Give the position of every Plasmodium parasite visible.
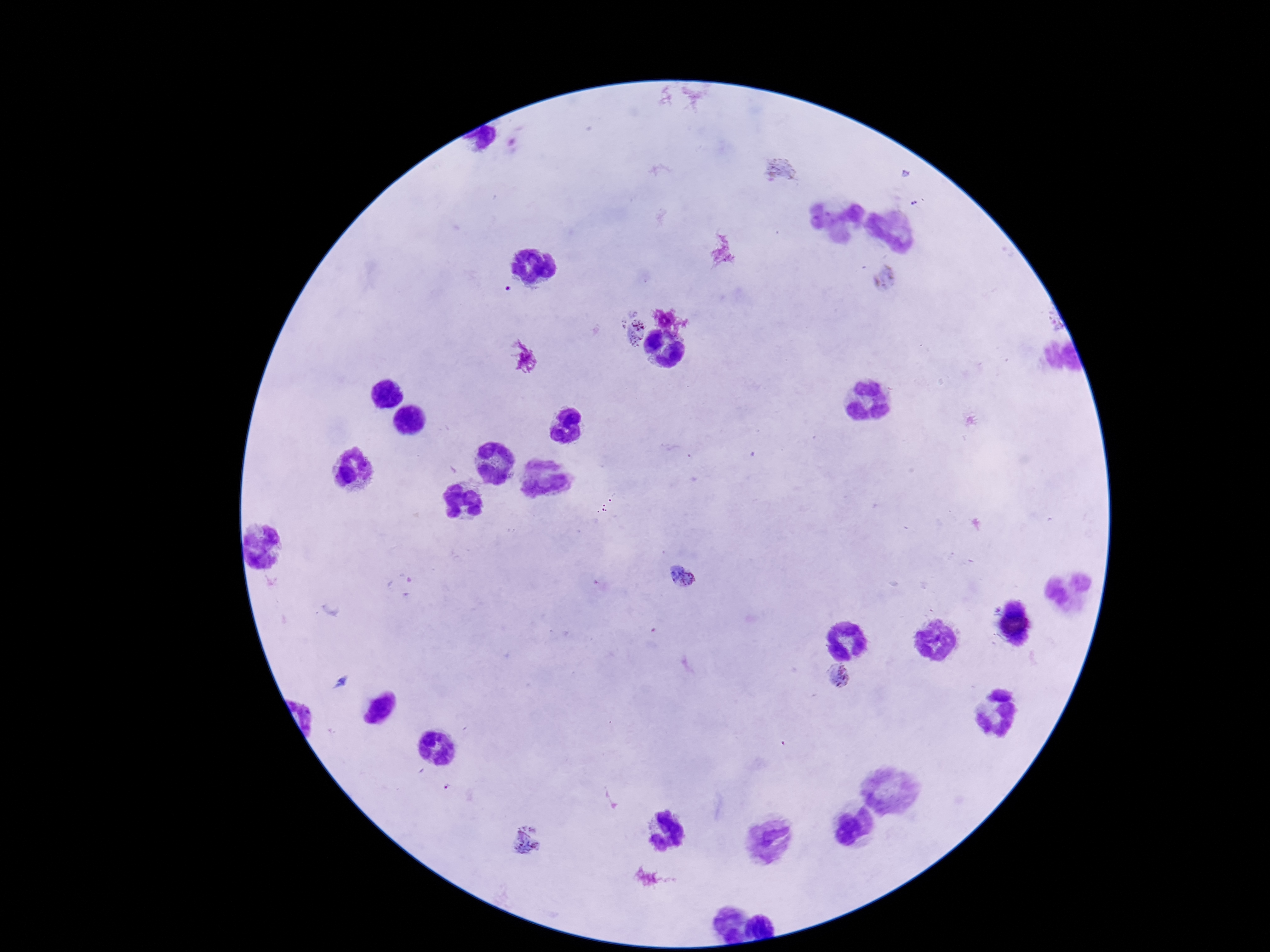

Approximate object centers, in pixels from the top-left corner.
Plasmodium parasites: (x=780, y=170), (x=885, y=277), (x=631, y=324), (x=684, y=578), (x=836, y=680), (x=526, y=842).

Summary:
  - Magnification: 100x
  - Image size: 1270×952 pixels
  - Patient malaria status: infected
  - Preparation: thick blood smear
  - Stain: Giemsa
  - Capture: smartphone camera through the microscope eyepiece
  - Field of view: single